Assess this cell for malaria.
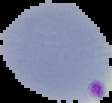

Parasitized.

Image is 112×103 pixels. From a thin blood smear. Cell region segmented out of the field of view; the surrounding area is masked to black.